State the preparation type.
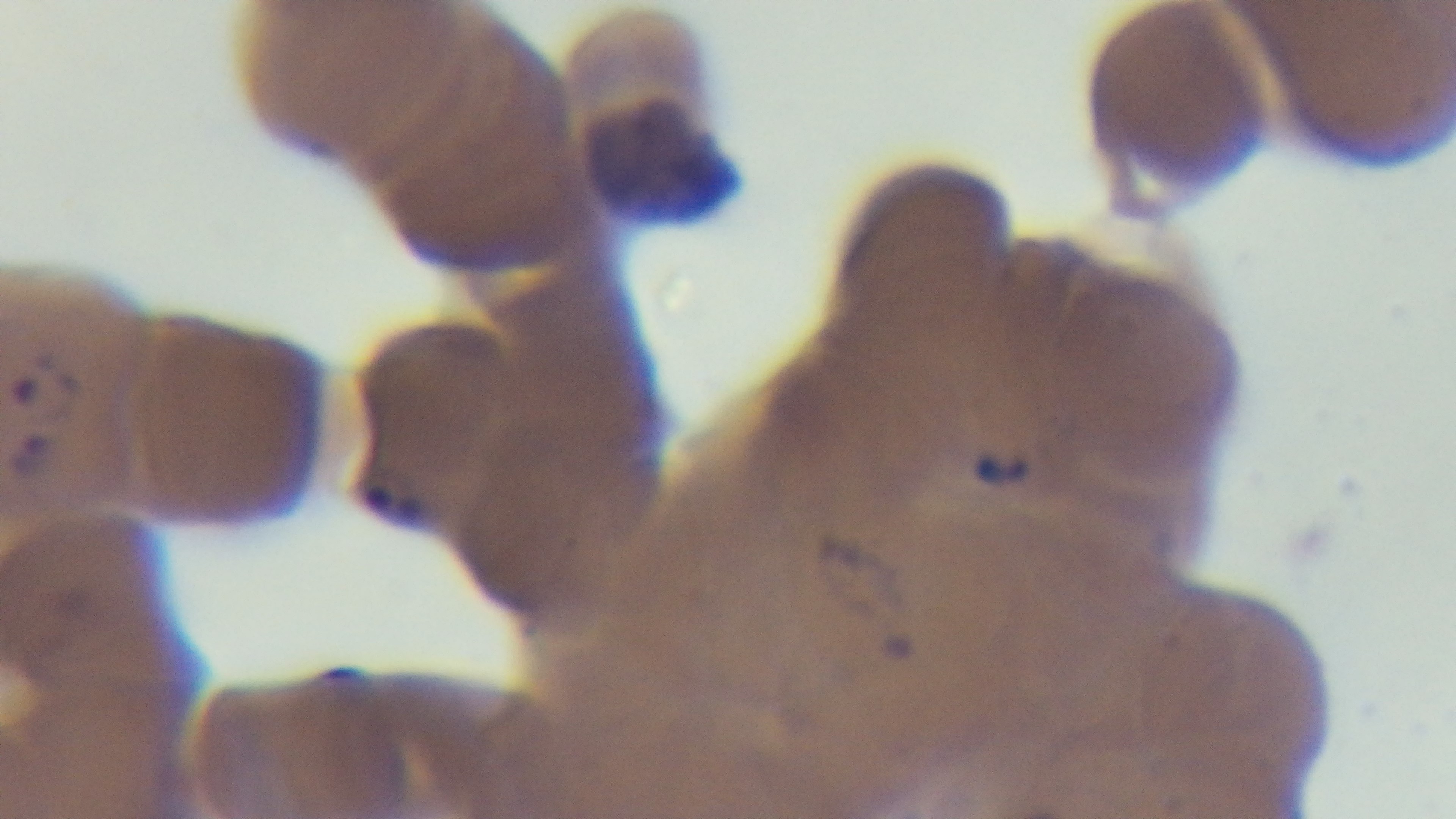

Thin.

One field from the slide. Malaria status: infected. Oil-immersion objective, 100x. Light microscopy. Giemsa-stained. Mounted 4K digital camera.